Look for Plasmodium parasites.
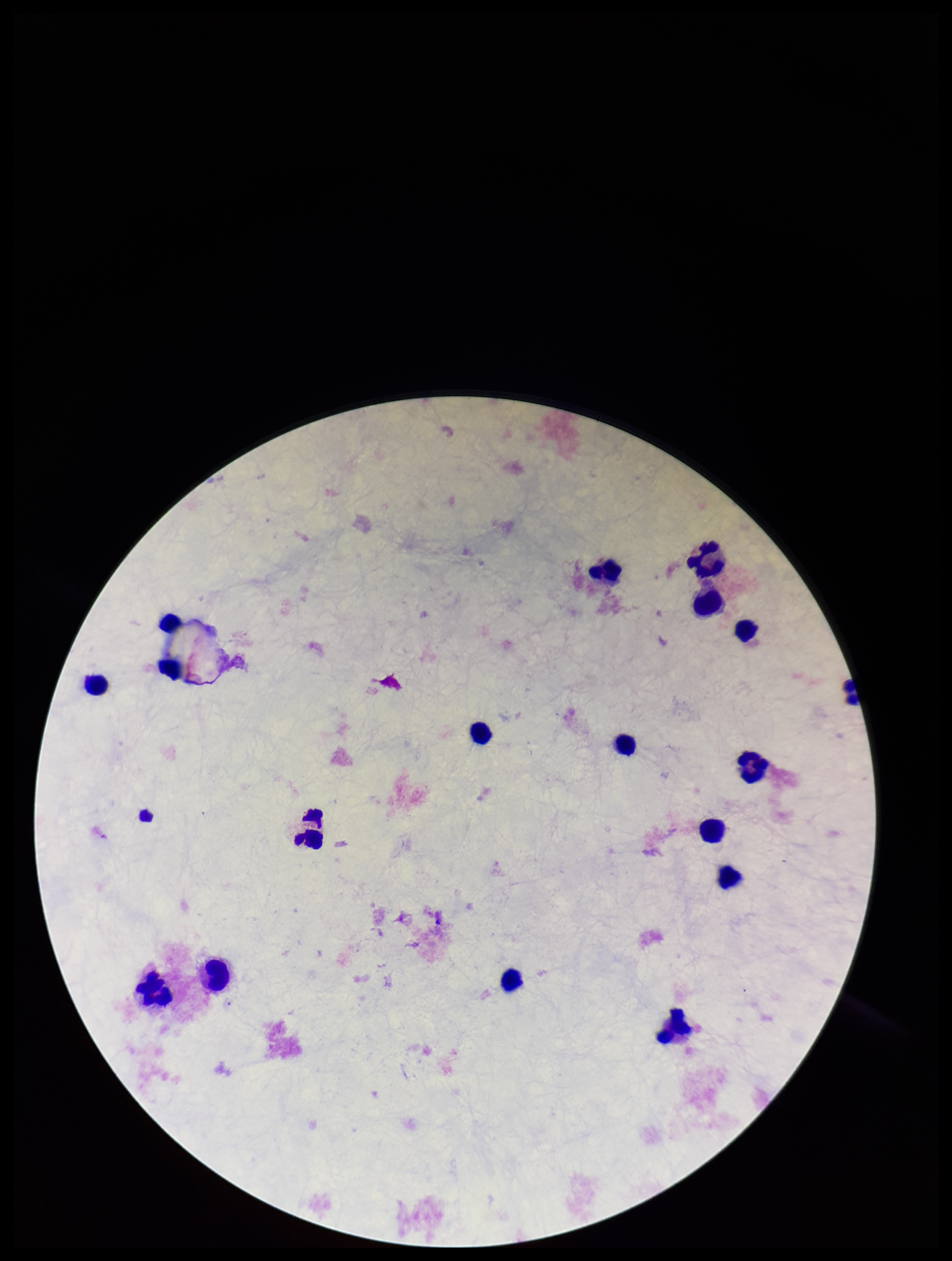
None seen.

preparation: thick smear
patient_malaria_status: negative
field_of_view: one from this slide
stain: Giemsa
leukocyte_count: 18
parasite_count: 0
image_size: 952×1261 pixels
capture: smartphone photograph through the microscope eyepiece